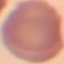

Malaria status: uninfected. Photographed with a smartphone camera at the microscope eyepiece. Giemsa stain. Automatically extracted cell patch, resized to 64 × 64 pixels. Thin smear of blood.